Outline each Plasmodium falciparum-infected red blood cell.
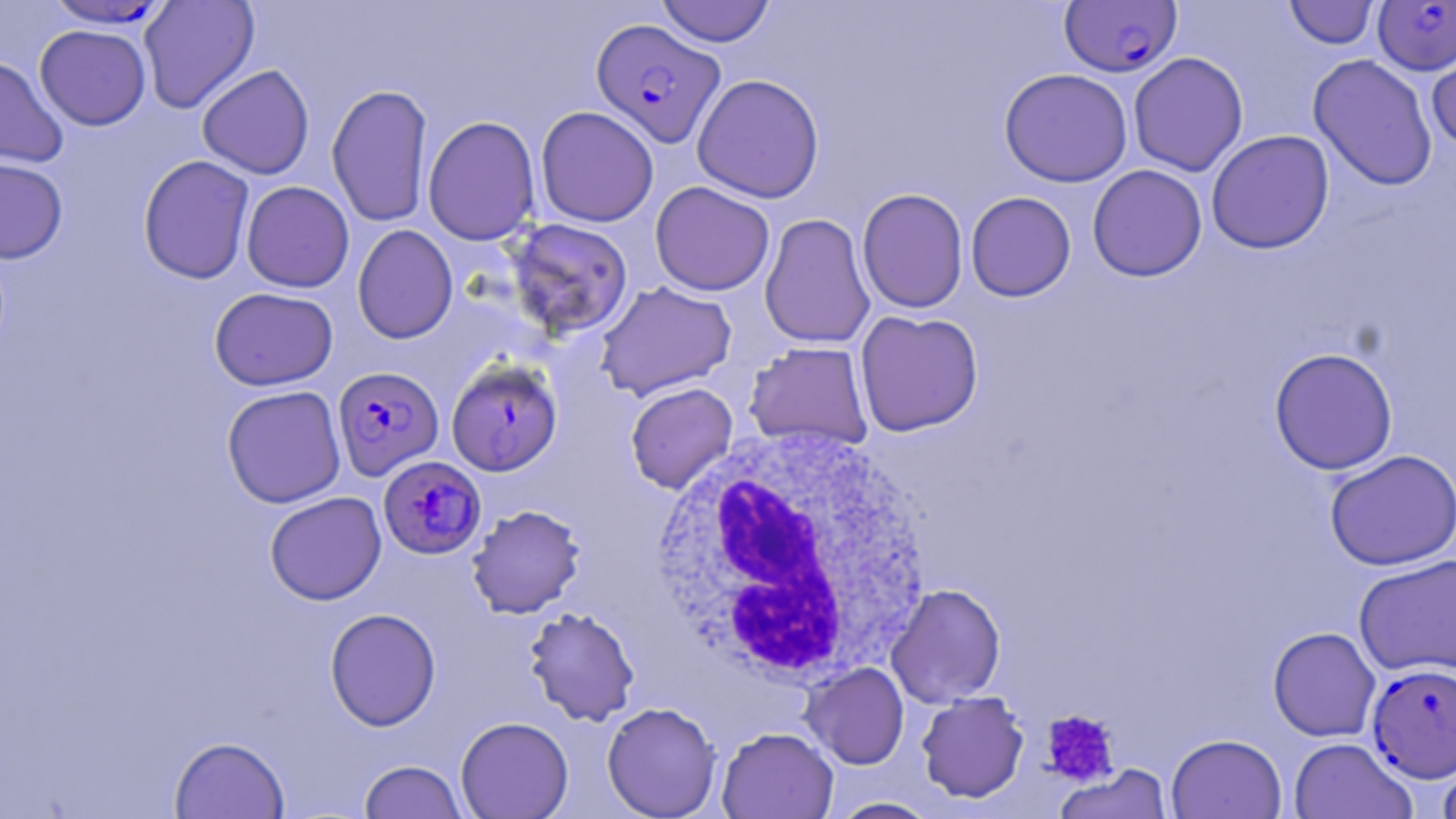
Approximate bounding boxes as named x1/y1/x2/y2 corners in pixels.
Plasmodium falciparum-infected red blood cells (subset): (x1=1059, y1=1, x2=1183, y2=77), (x1=1373, y1=1, x2=1456, y2=75), (x1=592, y1=18, x2=726, y2=147), (x1=332, y1=366, x2=444, y2=480), (x1=378, y1=455, x2=486, y2=559), (x1=1366, y1=662, x2=1456, y2=783).

Summary:
  - Uninfected red blood cell locations (subset): (x1=656, y1=0, x2=776, y2=47), (x1=42, y1=1, x2=173, y2=29), (x1=138, y1=1, x2=260, y2=113), (x1=1283, y1=1, x2=1381, y2=49), (x1=34, y1=24, x2=152, y2=130), (x1=1425, y1=38, x2=1456, y2=153), (x1=1128, y1=51, x2=1249, y2=177), (x1=1307, y1=53, x2=1438, y2=192), (x1=0, y1=56, x2=68, y2=168), (x1=197, y1=64, x2=314, y2=179), (x1=998, y1=68, x2=1133, y2=187), (x1=692, y1=73, x2=825, y2=203), (x1=327, y1=83, x2=433, y2=228), (x1=535, y1=106, x2=659, y2=227), (x1=423, y1=115, x2=541, y2=245), (x1=1206, y1=130, x2=1334, y2=254), (x1=137, y1=154, x2=255, y2=284), (x1=0, y1=156, x2=68, y2=264), (x1=1087, y1=164, x2=1207, y2=282), (x1=241, y1=181, x2=354, y2=292), (x1=650, y1=181, x2=775, y2=296), (x1=856, y1=188, x2=969, y2=313), (x1=965, y1=191, x2=1076, y2=302), (x1=759, y1=213, x2=875, y2=348), (x1=504, y1=218, x2=634, y2=340), (x1=352, y1=224, x2=458, y2=344), (x1=594, y1=280, x2=737, y2=401), (x1=209, y1=286, x2=338, y2=391), (x1=854, y1=309, x2=984, y2=437), (x1=744, y1=341, x2=874, y2=451), (x1=1269, y1=347, x2=1399, y2=475), (x1=625, y1=382, x2=738, y2=494), (x1=221, y1=385, x2=346, y2=508), (x1=1324, y1=449, x2=1456, y2=571), (x1=264, y1=491, x2=387, y2=605), (x1=466, y1=504, x2=586, y2=619), (x1=1353, y1=554, x2=1456, y2=677), (x1=886, y1=583, x2=1006, y2=707), (x1=523, y1=606, x2=640, y2=726), (x1=324, y1=607, x2=441, y2=731), (x1=1268, y1=627, x2=1380, y2=742), (x1=800, y1=662, x2=910, y2=769), (x1=916, y1=691, x2=1030, y2=803), (x1=602, y1=701, x2=721, y2=818), (x1=455, y1=716, x2=574, y2=818), (x1=716, y1=726, x2=838, y2=819), (x1=1166, y1=733, x2=1287, y2=819), (x1=169, y1=735, x2=290, y2=818), (x1=1288, y1=737, x2=1417, y2=819), (x1=1436, y1=752, x2=1456, y2=819), (x1=358, y1=760, x2=468, y2=818), (x1=1053, y1=764, x2=1173, y2=819), (x1=826, y1=797, x2=943, y2=818)
  - Platelet locations: (x1=1040, y1=709, x2=1120, y2=786)
  - White blood cell locations: (x1=643, y1=422, x2=938, y2=685)
  - Slide-level diagnosis: Plasmodium falciparum
  - Image size: 1456×819 pixels
  - Preparation: thin blood film
  - Modality: optical microscopy
  - Magnification: 1000x
  - Stain: May-Grünwald-Giemsa
  - Field of view: single